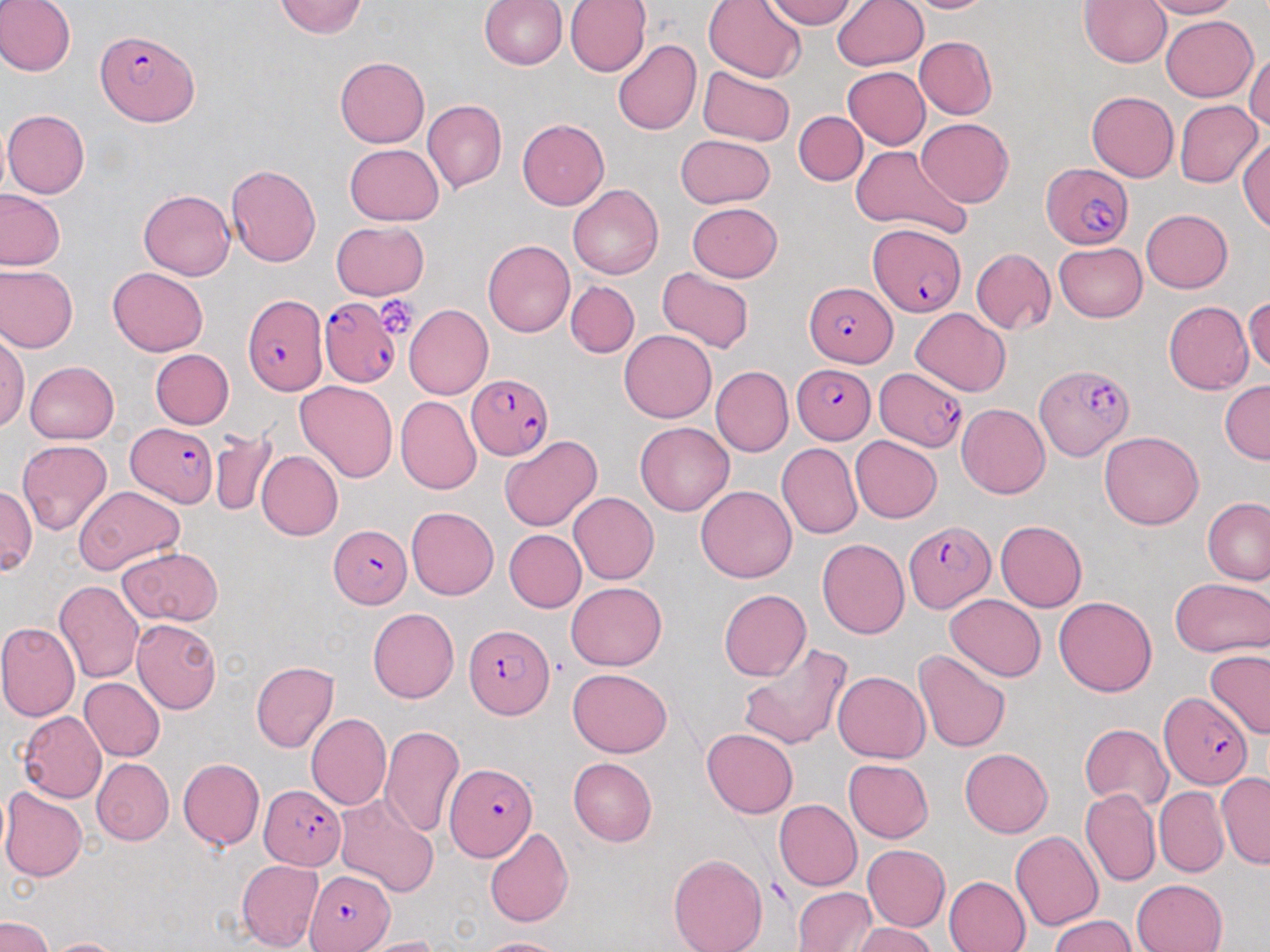

slide-level diagnosis = Plasmodium falciparum
preparation = thin blood smear
field of view = one of a larger specimen
uninfected red blood cell locations = approximate bounding boxes as (x1,y1)-(x2,y2) corner pairs in pixels: (0,0)-(76,77), (274,0)-(367,38), (565,0)-(650,76), (764,0)-(857,30), (832,0)-(928,71), (901,0)-(995,12), (1080,0)-(1171,67), (1144,0)-(1239,19), (478,1)-(566,70), (703,1)-(807,83), (1162,15)-(1258,102), (914,36)-(997,119), (612,39)-(701,136), (1247,47)-(1270,134), (335,57)-(429,147), (697,65)-(797,146), (841,67)-(930,149), (1086,91)-(1179,182), (422,100)-(506,194), (1175,100)-(1262,187), (3,110)-(90,198), (795,111)-(867,185), (916,117)-(1014,208), (517,118)-(609,209), (675,135)-(775,207), (1237,137)-(1270,233), (343,143)-(444,226), (851,145)-(972,239), (225,165)-(322,267), (568,183)-(663,279), (138,189)-(235,279), (0,190)-(65,271), (127,191)-(221,357), (687,202)-(782,281), (1141,209)-(1232,293), (330,220)-(429,300), (483,240)-(575,338), (1054,242)-(1147,322), (971,247)-(1056,335), (1,266)-(77,353), (107,268)-(208,356), (656,268)-(754,353), (565,281)-(639,358), (1245,296)-(1270,374), (1162,302)-(1254,392), (405,304)-(493,400), (911,307)-(1012,396), (620,330)-(717,422), (0,334)-(28,432), (150,349)-(234,429), (25,361)-(119,444), (710,365)-(793,456), (294,380)-(398,483), (1219,380)-(1270,464), (396,396)-(481,496), (956,403)-(1051,498), (635,422)-(734,516), (208,426)-(278,518), (1099,431)-(1204,529), (499,434)-(601,532), (850,436)-(941,524), (18,440)-(112,536), (776,442)-(863,539), (256,450)-(343,541), (75,485)-(184,575), (0,486)-(36,576), (695,486)-(798,583), (568,492)-(659,584), (1203,498)-(1270,585), (406,506)-(499,600), (995,520)-(1087,612), (505,530)-(586,612), (816,539)-(909,639), (120,546)-(223,627), (1192,577)-(1269,734), (1171,578)-(1270,658), (54,580)-(144,684), (566,581)-(666,671), (719,589)-(811,680), (944,594)-(1046,681), (1054,595)-(1157,697), (368,607)-(459,703), (131,618)-(221,714), (0,621)-(80,721), (738,643)-(853,750), (913,649)-(1012,755), (1205,651)-(1270,739), (250,660)-(338,752), (568,668)-(672,757), (833,671)-(930,763), (78,677)-(165,761), (18,711)-(107,802), (306,714)-(390,810), (1078,723)-(1172,813), (379,726)-(465,838), (701,727)-(798,819), (959,748)-(1052,838), (91,757)-(174,845), (568,757)-(657,846), (178,758)-(265,850), (843,758)-(934,842), (1217,772)-(1270,869), (1154,786)-(1229,877), (0,787)-(87,881), (1080,788)-(1160,888), (335,794)-(440,898), (773,799)-(863,891), (484,827)-(573,928), (1011,829)-(1103,932), (863,844)-(949,931), (668,852)-(767,952), (237,859)-(323,952), (944,875)-(1031,952), (1131,879)-(1227,952), (792,887)-(875,951), (0,914)-(54,952), (1047,915)-(1135,951), (851,922)-(937,952), (353,936)-(444,952), (42,937)-(129,952), (475,937)-(570,952)
image size = 1270×952 pixels
stain = May-Grünwald-Giemsa
platelet locations = approximate bounding boxes as (x1,y1)-(x2,y2) corner pairs in pixels: (375,295)-(422,337)
Plasmodium falciparum-infected red blood cell locations = approximate bounding boxes as (x1,y1)-(x2,y2) corner pairs in pixels: (97,29)-(198,127), (1040,164)-(1134,249), (868,224)-(966,318), (805,284)-(893,365), (242,292)-(328,396), (315,294)-(397,387), (1034,363)-(1134,461), (792,364)-(876,444), (875,366)-(969,452), (465,374)-(553,461), (126,423)-(218,507), (903,521)-(995,611), (330,523)-(411,606), (464,623)-(554,720), (1159,693)-(1251,789), (447,763)-(538,863), (258,785)-(346,869), (304,868)-(395,952)
modality = light microscopy
magnification = 1000x